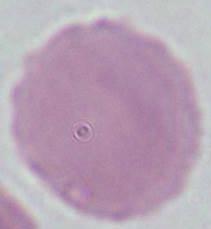
1000x magnification. A red blood cell is seen. Micrograph.